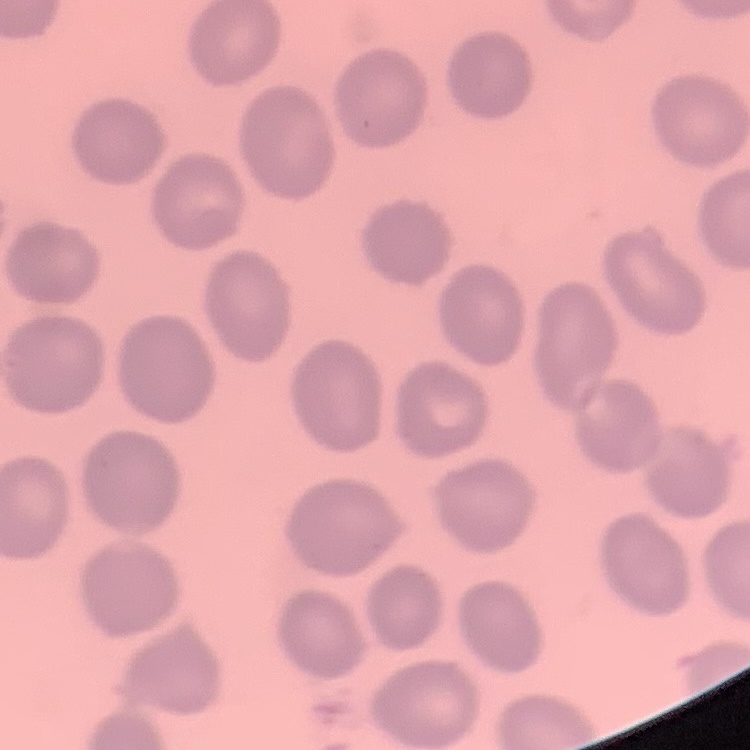

erythrocyte morphology = no rouleaux formation
image type = one tile cut from a larger photomicrograph
preparation = thin peripheral smear
stain = Field's or Giemsa